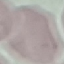 Result: no malaria parasites detected. Thin smear of blood. Acquired by smartphone through the microscope eyepiece. Automatically extracted cell patch, resized to 64 × 64 pixels. Giemsa stain.